Classify this cell by malaria status.
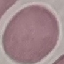
It is uninfected.

Summary:
  - Preparation: thin blood film
  - Capture: smartphone through the microscope eyepiece
  - Image type: automatically extracted cell patch, resized to 64 × 64 pixels
  - Stain: Giemsa